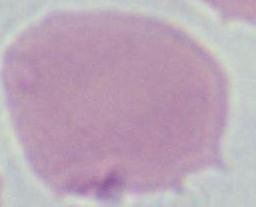
Micrograph. Captured at 1000x magnification. A red blood cell is shown.